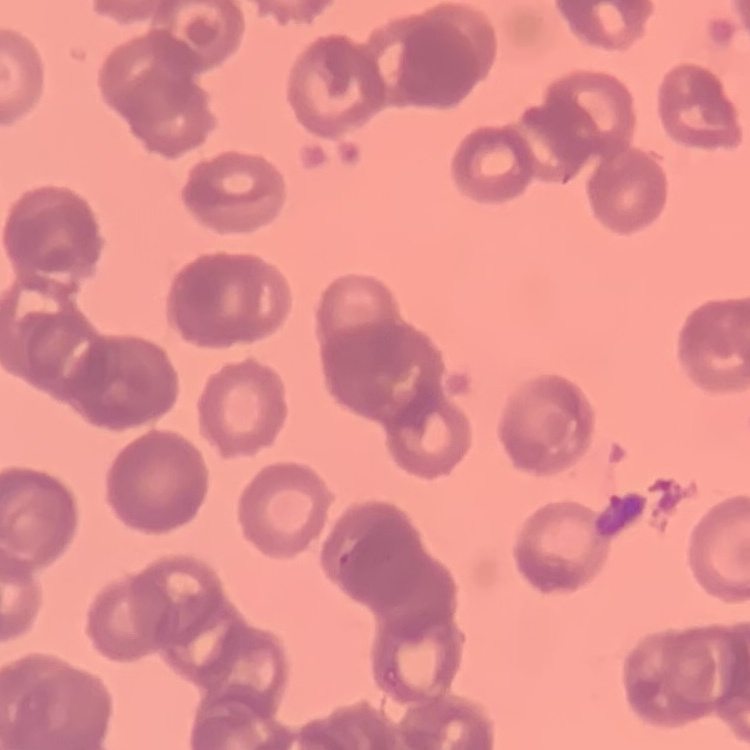

Summary:
  - Erythrocyte morphology: rouleaux formation
  - Preparation: thin blood smear
  - Image type: one tile cut from a larger photomicrograph
  - Stain: Field's or Giemsa